Locate every blood parasite and identify its species.
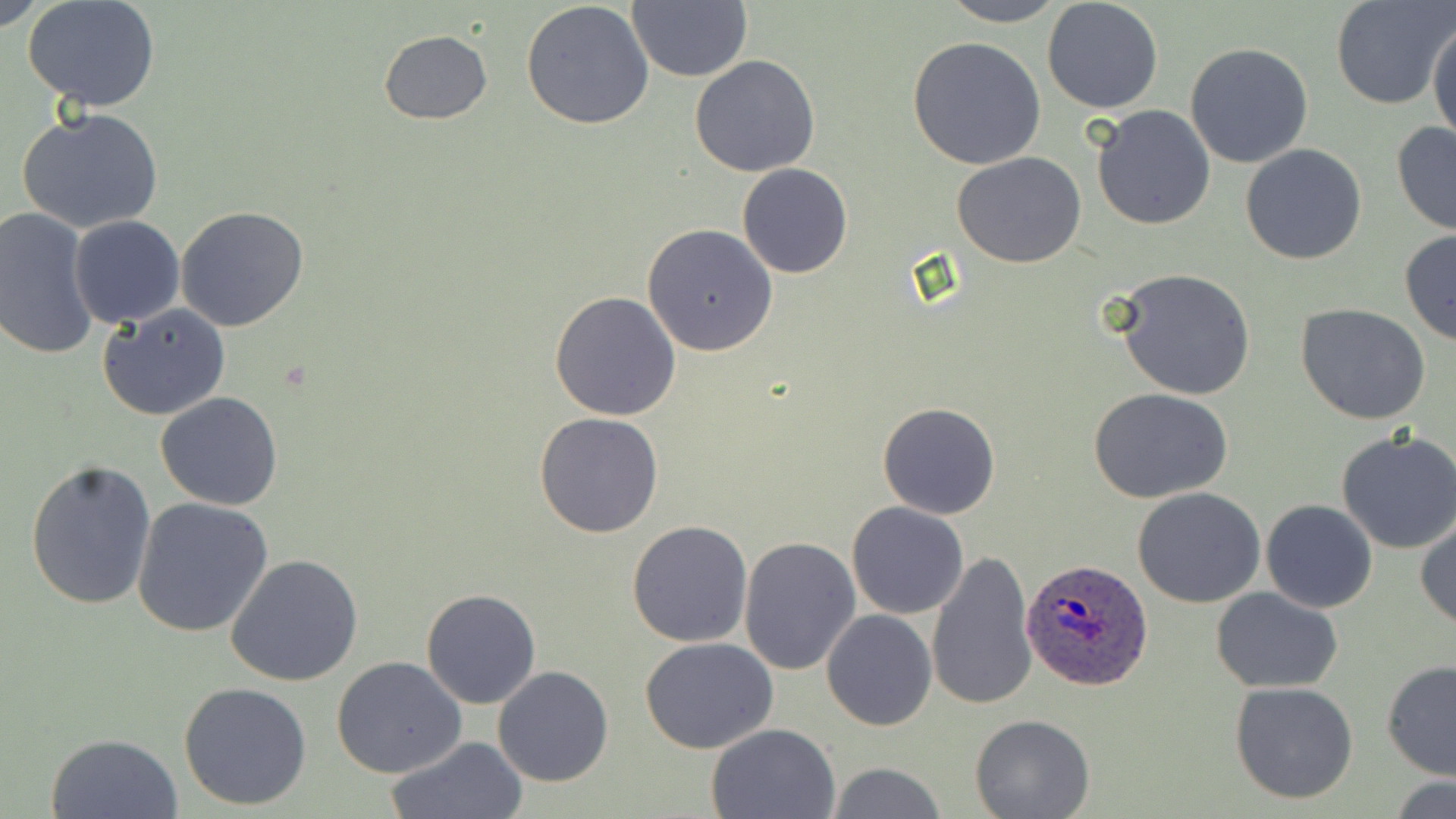
Approximate bounding boxes as (x1, y1, x2, y2) in pixels.
Plasmodium ovale-infected red blood cells: (1019, 558, 1153, 690).
No Plasmodium falciparum, Plasmodium malariae, Plasmodium vivax, Babesia divergens, or Trypanosoma brucei observed.

Uninfected red blood cell locations: (0, 0, 51, 30), (626, 0, 750, 84), (1042, 0, 1164, 115), (1328, 0, 1452, 111), (24, 1, 162, 112), (936, 1, 1069, 26), (520, 2, 654, 132), (1427, 18, 1455, 148), (378, 30, 492, 125), (907, 37, 1046, 171), (1185, 43, 1314, 168), (690, 54, 821, 177), (1092, 105, 1215, 230), (16, 107, 164, 234), (1390, 121, 1456, 235), (1240, 143, 1368, 265), (951, 151, 1086, 268), (737, 163, 852, 279), (175, 206, 308, 332), (1, 207, 99, 362), (69, 215, 186, 327), (643, 223, 780, 357), (1399, 230, 1456, 346), (1111, 268, 1256, 401), (549, 291, 681, 421), (98, 303, 231, 420), (1296, 303, 1431, 424), (1088, 387, 1234, 503), (157, 392, 282, 510), (878, 401, 1000, 519), (534, 412, 664, 538), (1335, 430, 1456, 555), (25, 458, 156, 611), (1132, 487, 1266, 608), (132, 497, 274, 638), (1261, 499, 1378, 614), (846, 501, 969, 619), (1416, 517, 1456, 630), (626, 520, 753, 648), (737, 534, 861, 675), (926, 549, 1037, 713), (225, 554, 366, 688), (1211, 587, 1345, 693), (422, 589, 541, 709), (822, 609, 937, 731), (641, 638, 779, 754), (332, 656, 466, 778), (1381, 660, 1456, 780), (492, 666, 614, 787), (1229, 680, 1359, 804), (178, 681, 312, 811), (970, 714, 1094, 819), (706, 722, 843, 818), (45, 732, 184, 819), (386, 737, 527, 818), (826, 762, 948, 818), (1386, 775, 1456, 818). Slide-level diagnosis: Plasmodium ovale. 1000x magnification. Optical microscopy. Image is 1456×819 pixels. Thin blood smear. May-Grünwald-Giemsa stain. One field of a larger specimen.